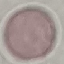

malaria status = uninfected
image type = cell patch, automatically extracted from a larger field of view and resized to 64 × 64 pixels
capture = smartphone through the microscope eyepiece
preparation = thin smear
stain = Giemsa